Locate and identify every blood parasite.
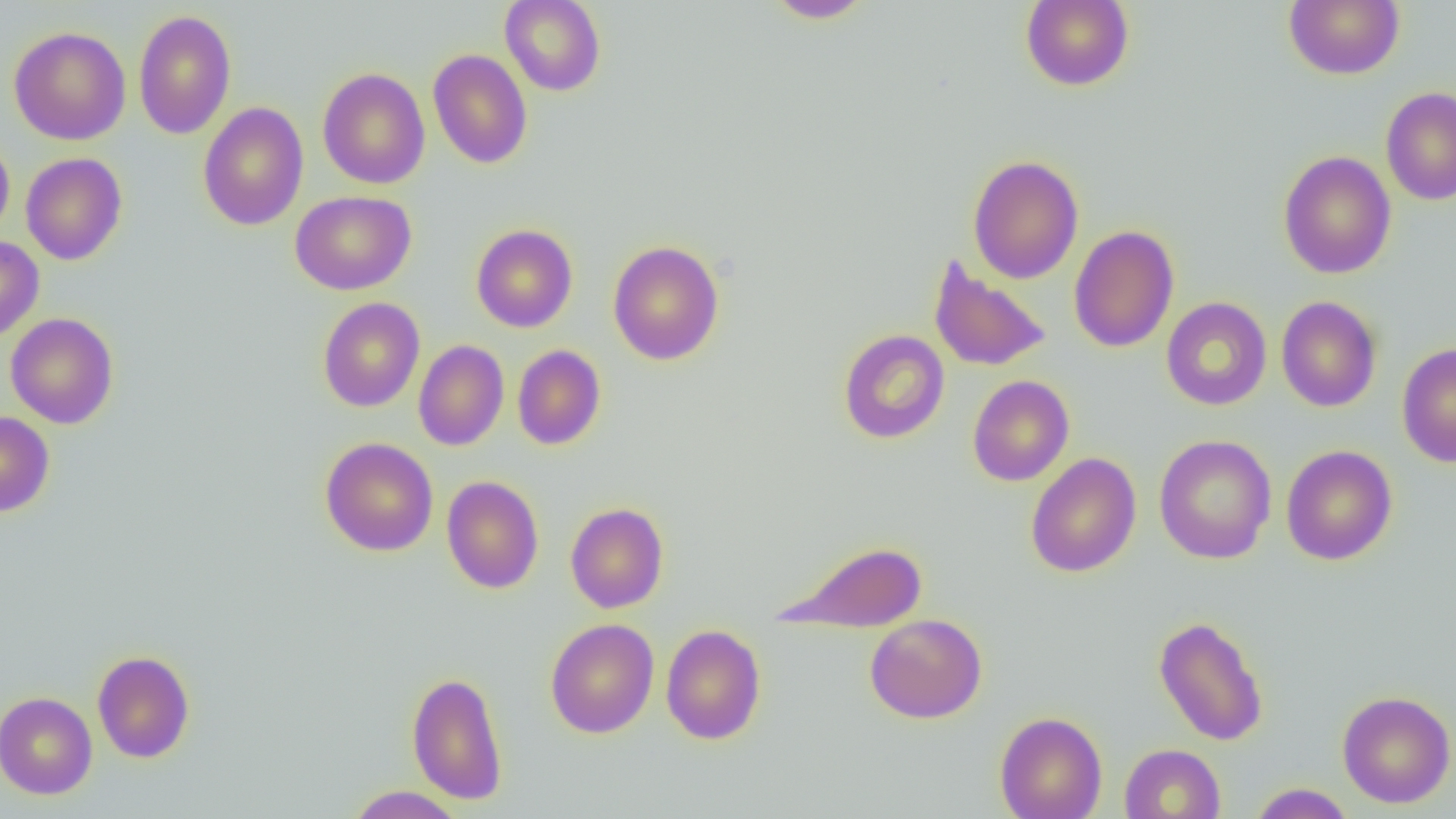

No blood parasites seen.

slide_level_diagnosis: no evidence of blood parasites
preparation: thin blood smear
field_of_view: single
magnification: 1000x
uninfected_red_blood_cell_locations: 'approximate bounding boxes as (x1,y1)-(x2,y2) corner pairs in pixels: (500,0)-(606,96), (764,0)-(876,23), (1020,0)-(1135,91), (1284,0)-(1405,80), (133,10)-(236,139), (8,26)-(131,145), (428,49)-(533,169), (317,67)-(430,189), (1381,86)-(1456,206), (197,101)-(309,231), (0,134)-(15,241), (1278,150)-(1396,279), (20,153)-(127,265), (967,154)-(1084,284), (290,191)-(416,295), (471,224)-(578,332), (1068,225)-(1179,353), (0,236)-(45,341), (607,240)-(725,365), (929,256)-(1052,372), (1276,295)-(1382,413), (317,297)-(425,412), (1161,297)-(1272,411), (6,313)-(119,429), (838,329)-(950,444), (413,339)-(509,451), (1397,342)-(1456,467), (512,344)-(606,450), (967,375)-(1074,486), (0,411)-(55,517), (1153,434)-(1277,564), (320,437)-(439,557), (1280,445)-(1398,566), (1025,452)-(1141,578), (441,475)-(544,594), (565,502)-(669,613), (774,538)-(928,633), (864,613)-(987,723), (1153,615)-(1268,746), (545,618)-(659,739), (660,624)-(767,745), (92,650)-(195,763), (406,670)-(509,804), (1336,690)-(1456,808), (0,691)-(98,799), (994,711)-(1108,819), (1119,743)-(1226,819), (1249,783)-(1355,819), (345,785)-(466,818)'
modality: optical microscopy
image_size: 1456×819 pixels